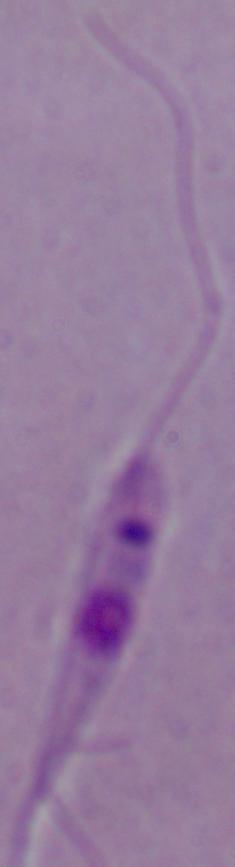 A Leishmania parasite is shown. Micrograph. 1000x magnification.